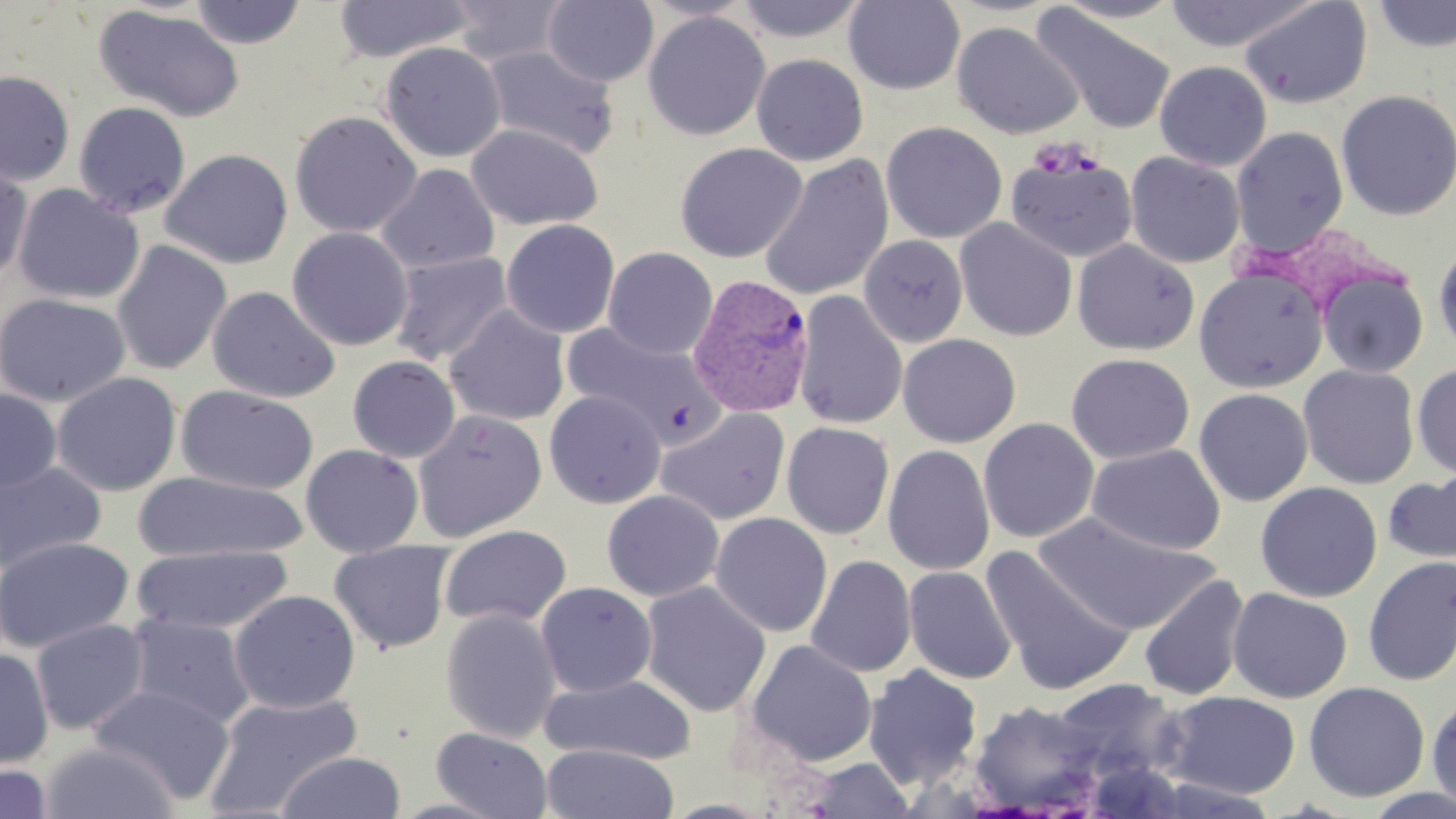
Summary:
  - Coordinate format: approximate bounding boxes as (x1,y1)-(x2,y2) corner pairs in pixels
  - Uninfected red blood cell locations: (543,0)-(658,87), (638,0)-(757,22), (732,0)-(869,43), (1052,0)-(1183,23), (1161,0)-(1323,52), (1238,0)-(1374,109), (189,1)-(307,49), (333,1)-(476,63), (446,1)-(572,66), (843,1)-(965,94), (1369,1)-(1456,53), (1030,4)-(1177,136), (93,6)-(246,123), (642,11)-(771,141), (951,21)-(1083,140), (379,42)-(505,163), (481,44)-(619,161), (751,53)-(869,166), (1154,60)-(1272,171), (0,70)-(75,186), (1335,89)-(1456,221), (73,101)-(191,219), (289,110)-(422,238), (881,122)-(1007,243), (466,123)-(603,231), (1230,126)-(1349,259), (674,142)-(808,263), (1005,147)-(1138,262), (160,149)-(293,269), (1125,151)-(1246,269), (758,155)-(894,301), (0,161)-(33,286), (376,163)-(499,274), (12,184)-(145,305), (954,218)-(1077,342), (501,219)-(621,338), (287,226)-(414,351), (859,235)-(969,347), (111,239)-(232,376), (1072,239)-(1199,356), (1432,240)-(1456,359), (602,246)-(718,359), (389,251)-(513,366), (1193,266)-(1329,393), (1316,268)-(1428,380), (207,286)-(340,403), (792,290)-(908,430), (0,292)-(130,408), (445,305)-(570,425), (561,321)-(725,446), (897,334)-(1021,447), (1066,352)-(1194,464), (347,355)-(460,462), (1412,362)-(1456,480), (1298,365)-(1420,489), (51,372)-(182,496), (176,386)-(319,495), (1193,388)-(1313,506), (0,389)-(61,491), (544,390)-(666,508), (655,407)-(791,525), (412,409)-(547,542), (978,418)-(1100,543), (781,422)-(895,539), (800,436)-(978,566), (1087,443)-(1226,556), (300,444)-(424,557), (882,445)-(995,576), (0,460)-(107,576), (1382,469)-(1456,570), (134,472)-(308,562), (1255,481)-(1382,602), (601,490)-(724,602), (710,512)-(833,637), (1032,513)-(1218,635), (439,525)-(572,629), (0,536)-(134,654), (329,540)-(455,654), (131,544)-(293,635), (981,546)-(1137,696), (805,554)-(916,678), (1362,556)-(1456,687), (903,566)-(1017,684), (1138,575)-(1250,701), (535,581)-(657,698), (639,581)-(772,718), (1227,587)-(1353,703), (228,589)-(361,714), (440,607)-(562,743), (125,613)-(256,729), (30,618)-(150,735), (743,639)-(877,768), (0,647)-(54,769), (863,664)-(983,790), (539,673)-(697,765), (1048,679)-(1186,787), (1303,681)-(1430,802), (88,683)-(236,806), (203,691)-(363,818), (1162,691)-(1301,797), (1426,692)-(1456,813), (967,700)-(1106,814), (430,727)-(554,819), (40,741)-(179,819), (541,744)-(679,819), (276,752)-(406,819), (799,758)-(916,818), (0,760)-(53,819), (660,798)-(777,818)
  - Plasmodium vivax-infected red blood cell locations: (687,273)-(816,418)
  - Slide-level diagnosis: Plasmodium vivax
  - Preparation: thin blood film
  - Magnification: 1000x
  - Stain: May-Grünwald-Giemsa
  - Modality: optical microscopy
  - Field of view: one of a larger specimen
  - Image size: 1456×819 pixels